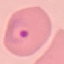

Summary:
  - Malaria status: parasitized
  - Preparation: thin blood smear
  - Stain: Giemsa
  - Capture: smartphone through the microscope eyepiece
  - Image type: automatically extracted cell patch, resized to 64 × 64 pixels